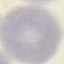

{
  "malaria_status": "uninfected",
  "image_type": "cell patch, automatically extracted from a larger field of view and resized to 64 × 64 pixels",
  "stain": "Giemsa",
  "capture": "smartphone through the microscope eyepiece",
  "preparation": "thin smear"
}